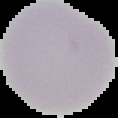

Summary:
  - Image type: cell region segmented out of the field of view; surrounding area masked to black
  - Preparation: thin blood smear
  - Image size: 118×118 pixels
  - Result: no Plasmodium parasites seen